Comment on the morphology of the red blood cells.
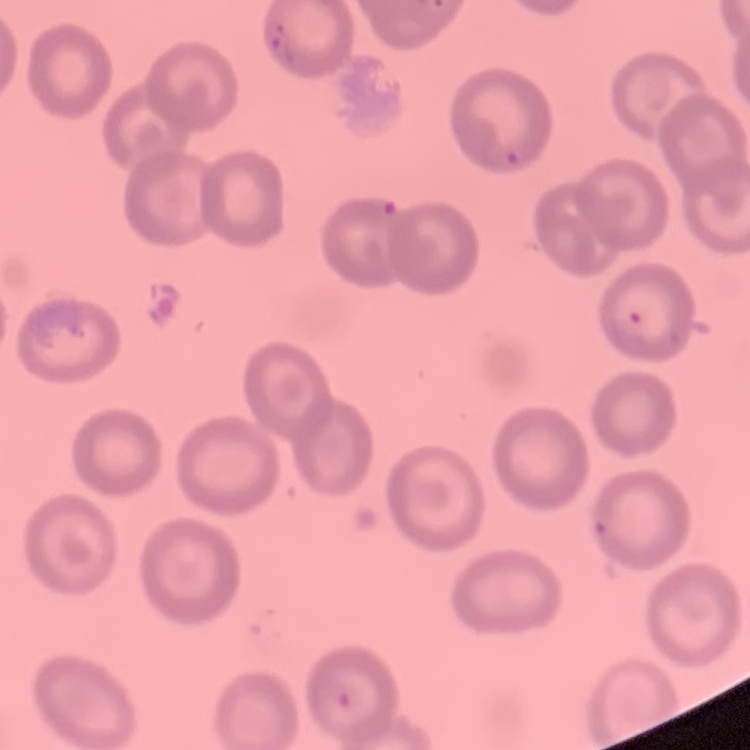

They show no rouleaux formation.

{
  "image_type": "square crop of a larger photomicrograph",
  "preparation": "thin blood smear",
  "stain": "Field's or Giemsa"
}